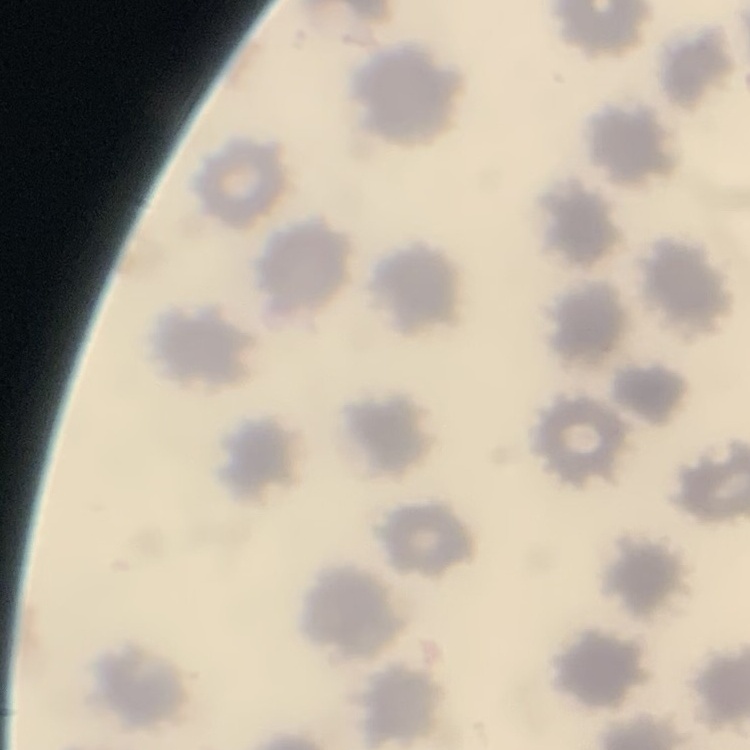

Summary:
  - Erythrocyte morphology: no rouleaux formation
  - Image type: one tile cut from a larger photomicrograph
  - Preparation: thin peripheral smear
  - Stain: Field's or Giemsa